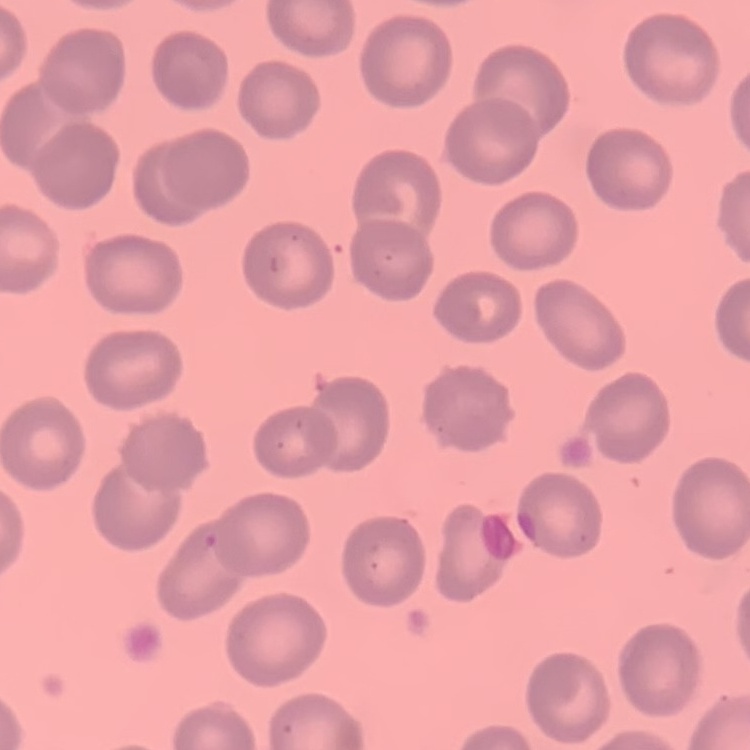
red blood cell morphology = no rouleaux formation
image type = square crop of a larger photomicrograph
preparation = thin peripheral smear
stain = Field's or Giemsa